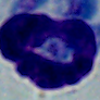
magnification = 1000x
identification = leukocyte
modality = micrograph